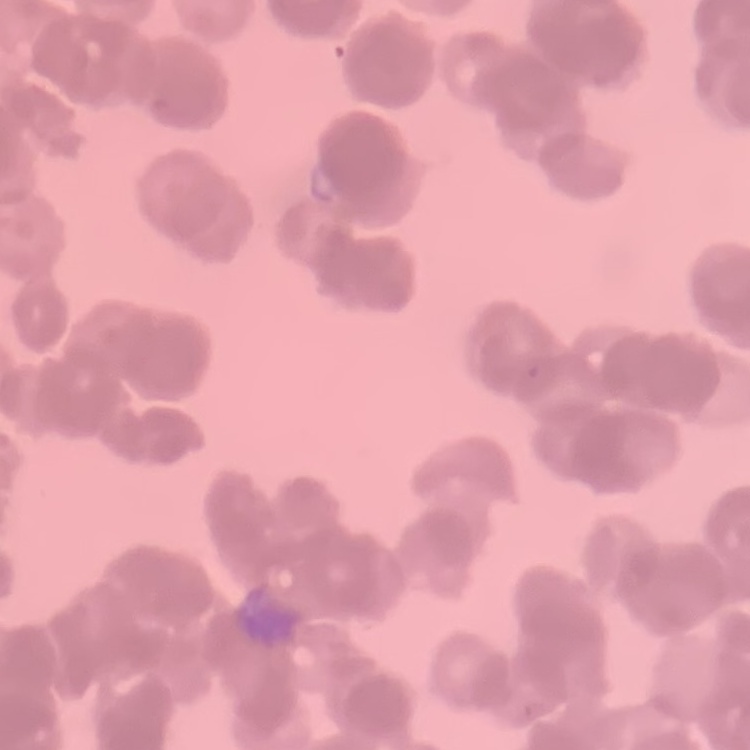
Summary:
  - Erythrocyte morphology: rouleaux formation
  - Stain: Field's or Giemsa
  - Preparation: thin blood film
  - Image type: one tile cut from a larger photomicrograph